Identify the parasite.
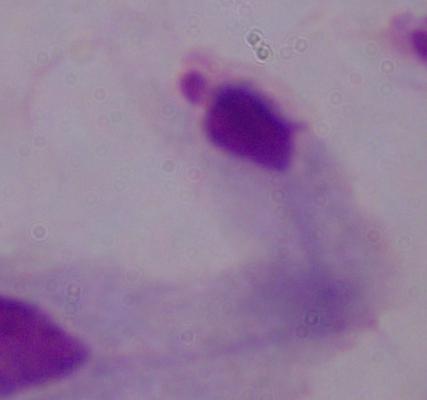

This is a trichomonad.

{
  "modality": "photomicrograph",
  "magnification": "1000x"
}